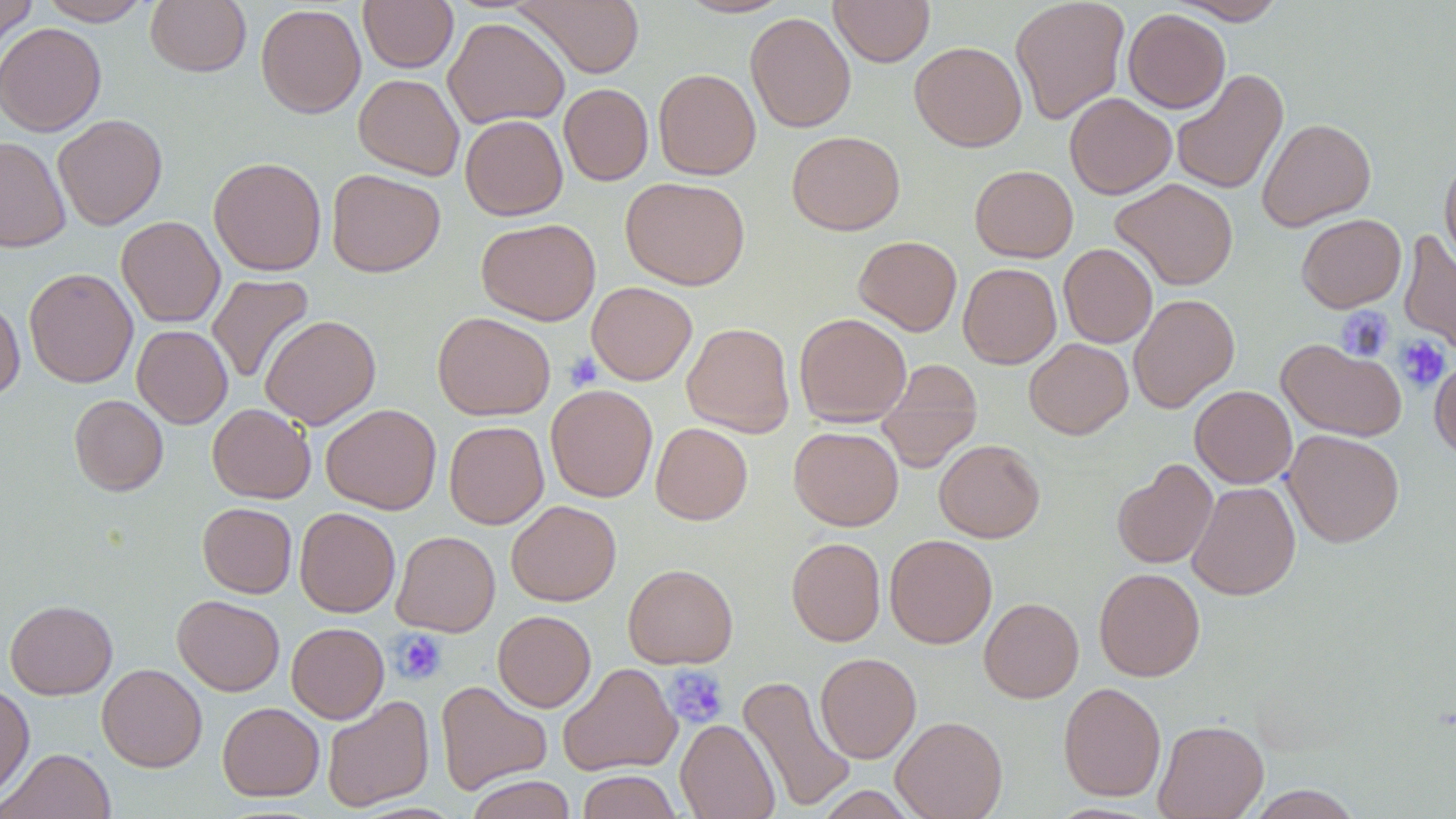

Summary:
  - Coordinate format: approximate bounding boxes as (x1,y1)-(x2,y2) corner pairs in pixels
  - Platelet locations: (1336,306)-(1395,362), (1394,334)-(1450,392), (564,351)-(602,390), (391,629)-(447,685), (663,666)-(730,729)
  - Uninfected red blood cell locations: (1,0)-(37,54), (38,0)-(152,25), (145,0)-(251,76), (358,0)-(458,73), (512,0)-(645,78), (676,0)-(793,19), (829,0)-(934,67), (1010,0)-(1130,125), (1169,0)-(1288,24), (255,4)-(366,118), (1123,9)-(1230,113), (745,12)-(856,133), (443,17)-(570,129), (0,22)-(106,136), (910,41)-(1027,152), (653,68)-(761,179), (1172,68)-(1288,195), (353,73)-(465,180), (559,83)-(653,185), (1064,92)-(1177,199), (53,114)-(167,230), (460,115)-(568,220), (1257,117)-(1376,232), (787,130)-(905,235), (0,136)-(70,252), (1439,154)-(1456,272), (208,157)-(326,275), (970,165)-(1078,263), (327,169)-(445,277), (620,176)-(751,290), (1110,178)-(1238,291), (1296,214)-(1406,313), (116,216)-(225,327), (476,218)-(601,325), (1398,230)-(1456,354), (853,235)-(962,336), (1058,243)-(1157,348), (958,263)-(1061,368), (24,268)-(138,388), (206,273)-(314,385), (586,282)-(697,385), (1129,294)-(1240,413), (0,297)-(25,399), (432,312)-(555,420), (794,313)-(911,426), (260,314)-(381,429), (682,322)-(795,437), (132,325)-(233,428), (1024,338)-(1133,439), (1277,338)-(1407,442), (1429,356)-(1456,460), (876,359)-(983,472), (545,384)-(658,502), (1190,385)-(1297,488), (69,395)-(168,495), (207,403)-(315,503), (321,404)-(441,515), (444,421)-(549,529), (651,422)-(752,524), (789,426)-(903,531), (1283,429)-(1404,547), (934,439)-(1046,542), (1111,459)-(1218,569), (1187,481)-(1300,600), (506,500)-(621,606), (198,502)-(297,598), (295,507)-(400,617), (392,530)-(500,636), (884,534)-(997,649), (786,537)-(886,646), (623,563)-(738,668), (1094,568)-(1205,681), (172,595)-(284,696), (979,597)-(1083,703), (5,599)-(117,700), (493,610)-(596,712), (286,622)-(389,723), (815,652)-(921,763), (97,663)-(207,772), (558,663)-(682,776), (736,675)-(856,812), (435,680)-(552,795), (0,681)-(35,803), (1058,682)-(1166,801), (322,695)-(434,812), (217,702)-(324,801), (891,715)-(1008,819), (675,719)-(780,819), (1154,719)-(1268,818), (2,748)-(116,819), (577,770)-(681,819), (465,775)-(577,819), (1245,785)-(1364,819), (814,786)-(919,818)
  - Slide-level diagnosis: negative for blood parasites
  - Stain: May-Grünwald-Giemsa
  - Preparation: thin blood smear
  - Image size: 1456×819 pixels
  - Modality: light microscopy
  - Field of view: one of a larger specimen
  - Magnification: 1000x